State the blood parasite species.
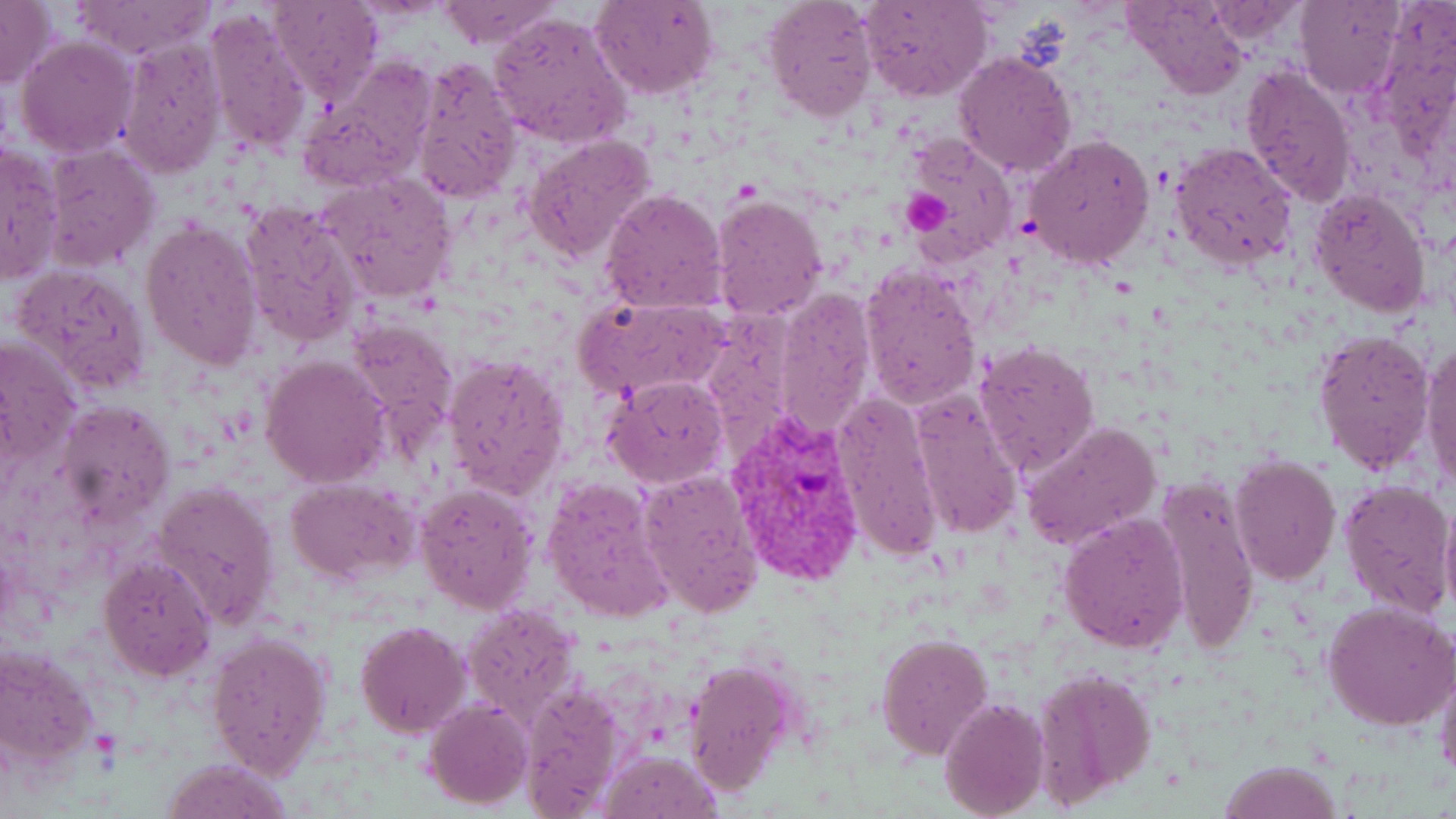
Plasmodium vivax.

Summary:
  - Coordinate format: approximate bounding boxes as (x1, y1, x2, y2) in pixels
  - Platelet locations: (901, 187, 955, 234)
  - Uninfected red blood cell locations: (268, 0, 381, 107), (433, 0, 562, 48), (589, 0, 718, 101), (860, 0, 990, 103), (1124, 0, 1245, 100), (1296, 0, 1406, 100), (0, 1, 55, 89), (760, 1, 878, 122), (71, 2, 214, 59), (1200, 3, 1308, 43), (204, 7, 316, 155), (489, 10, 634, 149), (16, 36, 138, 158), (117, 37, 227, 178), (953, 51, 1076, 177), (299, 57, 437, 190), (410, 57, 522, 202), (1239, 63, 1357, 206), (523, 133, 657, 263), (902, 133, 1017, 261), (1024, 133, 1154, 270), (1, 141, 63, 286), (1170, 141, 1298, 268), (42, 144, 161, 271), (538, 153, 725, 294), (316, 172, 457, 303), (1308, 188, 1432, 317), (600, 189, 728, 313), (710, 191, 830, 324), (238, 198, 365, 348), (141, 220, 266, 370), (858, 262, 982, 411), (14, 264, 152, 395), (775, 288, 876, 436), (574, 292, 733, 400), (343, 316, 460, 457), (1313, 330, 1436, 474), (1, 337, 82, 473), (1421, 339, 1455, 495), (973, 340, 1102, 477), (442, 353, 572, 499), (260, 355, 390, 487), (602, 375, 730, 489), (907, 387, 1024, 540), (833, 390, 946, 561), (55, 400, 175, 525), (1019, 420, 1163, 554), (1228, 455, 1342, 587), (638, 468, 765, 617), (541, 476, 676, 624), (1154, 476, 1264, 653), (284, 478, 417, 583), (1339, 478, 1454, 618), (150, 480, 281, 630), (413, 480, 540, 616), (1439, 496, 1456, 623), (1058, 511, 1190, 653), (98, 555, 216, 680), (1322, 599, 1456, 732), (461, 602, 582, 726), (355, 620, 471, 737), (207, 630, 333, 779), (875, 633, 994, 758), (0, 645, 99, 767), (1433, 649, 1456, 784), (684, 659, 799, 797), (1034, 666, 1158, 806), (513, 680, 630, 816), (938, 695, 1049, 819), (424, 699, 533, 808), (596, 749, 722, 819), (158, 758, 298, 818), (1217, 759, 1345, 818)
  - Plasmodium vivax-infected red blood cell locations: (727, 405, 870, 587)
  - Field of view: one of a larger specimen
  - Magnification: 1000x
  - Preparation: thin blood film
  - Image size: 1456×819 pixels
  - Stain: May-Grünwald-Giemsa
  - Modality: light microscopy